Evaluate for malaria.
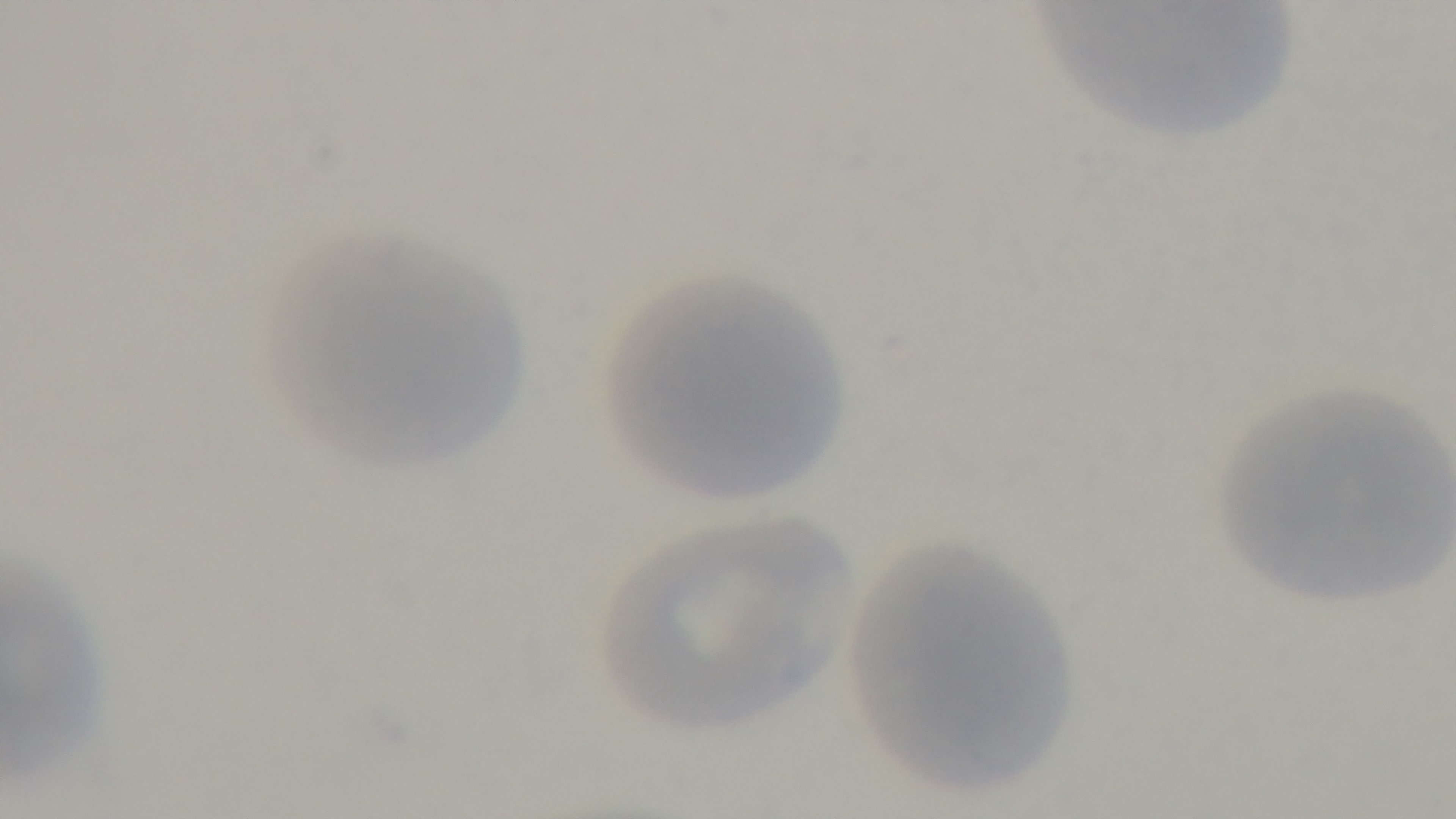

Negative.

One field from the slide. Captured with a mounted 4K digital camera. Photomicrograph. Giemsa-stained. 100x oil-immersion objective. Preparation: thin blood film.